Identify the parasite.
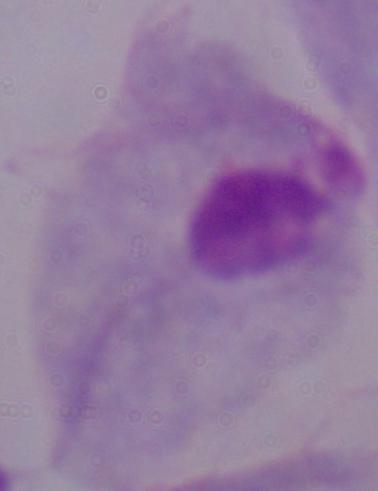

A trichomonad.

Summary:
  - Modality: photomicrograph
  - Magnification: 1000x